Evaluate for Plasmodium parasites.
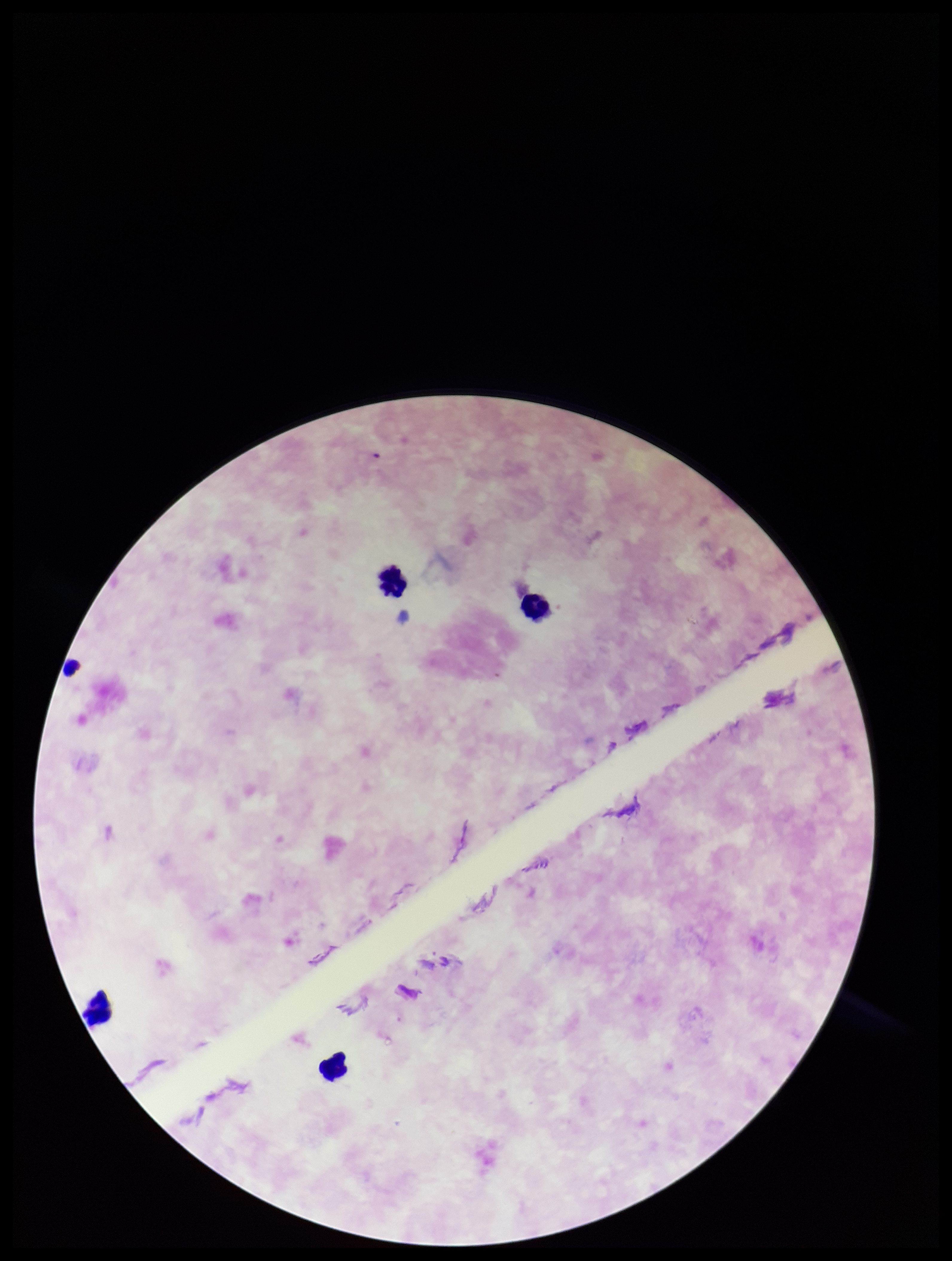
None detected.

field of view = one from this slide
preparation = thick blood smear
stain = Giemsa
leukocyte count = 4
parasite count = 0
patient malaria status = negative
capture = smartphone photograph through the microscope eyepiece
image size = 952×1261 pixels